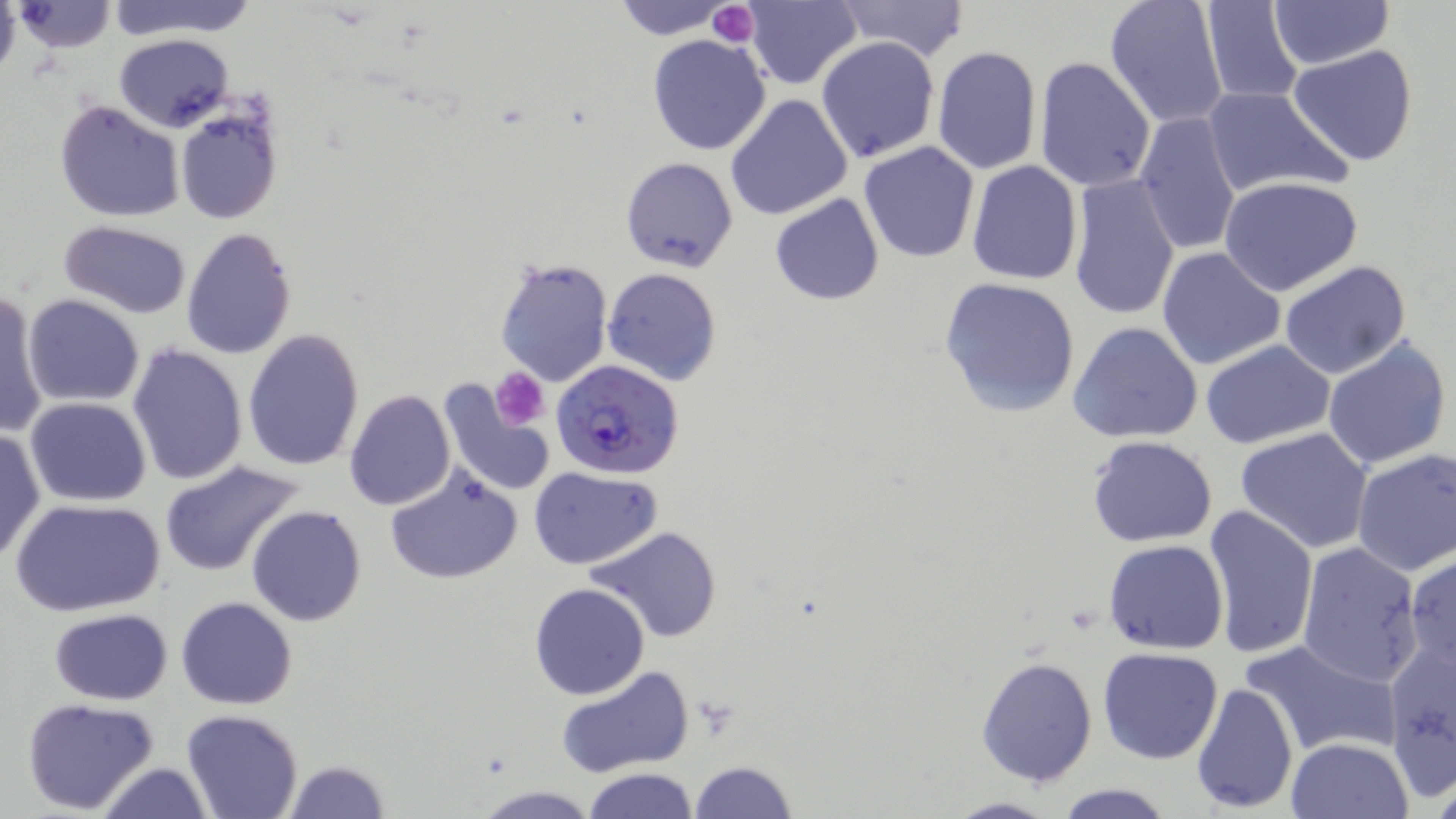
Summary:
  - Coordinate format: approximate bounding boxes as (x1,y1)-(x2,y2) corner pairs in pixels
  - Plasmodium falciparum-infected red blood cell locations: (553,360)-(682,479)
  - Uninfected red blood cell locations: (0,0)-(20,81), (103,0)-(259,41), (609,0)-(737,39), (743,0)-(862,89), (832,0)-(971,64), (1104,0)-(1230,129), (1268,0)-(1394,69), (13,1)-(118,53), (1198,1)-(1305,106), (115,34)-(235,133), (647,34)-(772,156), (816,37)-(940,161), (933,44)-(1043,177), (1287,44)-(1419,167), (1033,55)-(1157,193), (1201,85)-(1351,200), (725,94)-(853,221), (53,98)-(185,223), (175,103)-(283,225), (1135,111)-(1241,257), (858,141)-(980,263), (620,156)-(738,272), (966,160)-(1084,284), (1067,173)-(1182,321), (1221,177)-(1363,294), (769,193)-(885,307), (60,220)-(191,317), (182,226)-(297,360), (1157,247)-(1287,370), (494,256)-(613,388), (1278,260)-(1411,379), (603,268)-(722,385), (938,276)-(1080,416), (1,289)-(51,439), (22,295)-(144,406), (1068,321)-(1204,444), (242,328)-(364,471), (1321,335)-(1452,470), (1200,340)-(1337,451), (128,344)-(248,486), (437,376)-(556,499), (344,389)-(455,509), (25,397)-(152,506), (1234,428)-(1374,554), (0,429)-(44,562), (1086,435)-(1219,547), (1350,450)-(1456,577), (157,459)-(305,577), (385,466)-(524,585), (529,466)-(660,568), (11,497)-(165,617), (247,505)-(366,627), (1204,506)-(1318,662), (587,526)-(726,644), (1103,539)-(1228,654), (1295,540)-(1425,686), (1404,553)-(1455,674), (529,582)-(650,699), (177,597)-(298,709), (49,609)-(174,705), (1242,636)-(1399,759), (1386,637)-(1455,793), (1096,646)-(1224,764), (976,656)-(1098,787), (557,664)-(694,777), (1192,681)-(1298,813), (22,697)-(161,815), (181,710)-(304,819), (1284,736)-(1414,819), (281,759)-(393,817), (686,759)-(797,819), (95,762)-(217,818), (582,768)-(698,818), (1052,781)-(1175,818), (474,784)-(596,817), (942,796)-(1061,818)
  - Platelet locations: (707,2)-(759,48), (491,369)-(549,428)
  - Slide-level diagnosis: Plasmodium falciparum
  - Image size: 1456×819 pixels
  - Field of view: single
  - Modality: optical microscopy
  - Stain: May-Grünwald-Giemsa
  - Preparation: thin blood film
  - Magnification: 1000x